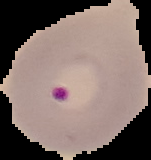

result = Plasmodium parasites detected
image size = 151×160 pixels
image type = segmented cell region on a black background
preparation = thin blood smear